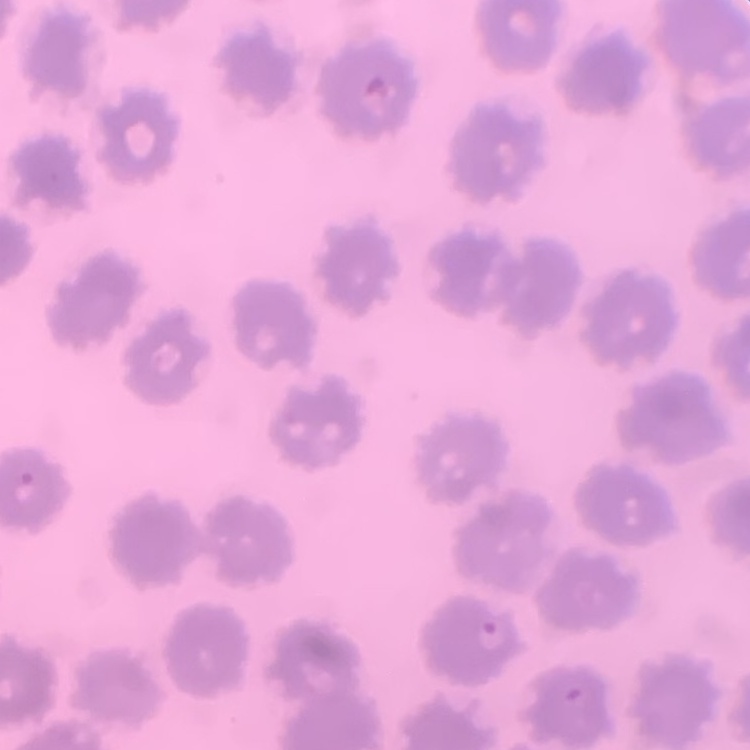

Summary:
  - Red blood cell morphology: no rouleaux formation
  - Image type: one tile cut from a larger photomicrograph
  - Stain: Field's or Giemsa
  - Preparation: thin blood smear